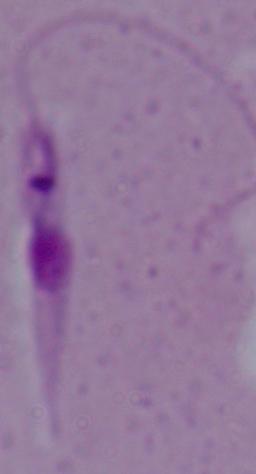 A Leishmania parasite is seen. Captured at 1000x magnification. Micrograph.